Point out each malaria parasite.
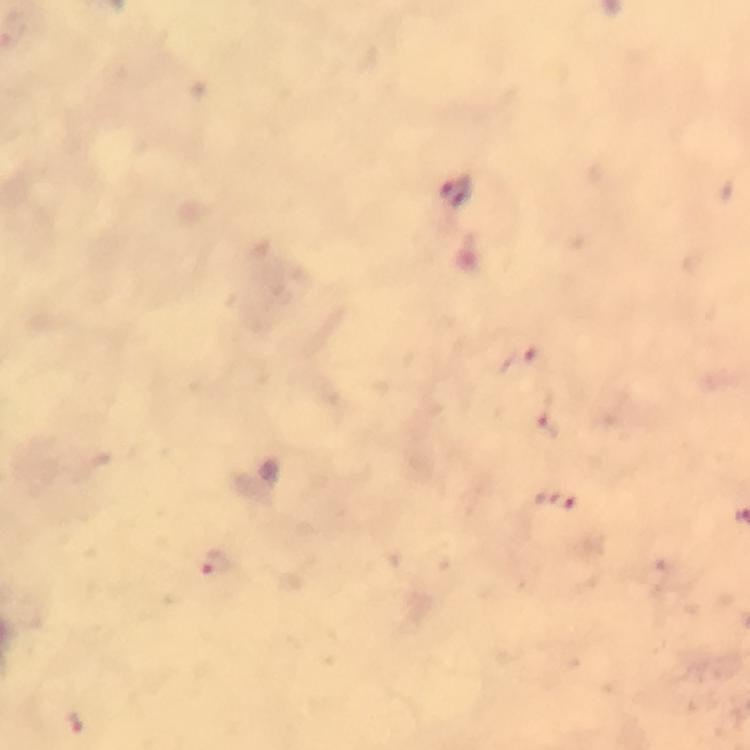
Approximate centers as (x, y) in pixels.
Malaria parasites: (457, 195), (521, 361), (546, 417), (557, 501), (215, 564), (73, 723).

Photographed with a smartphone mounted on the microscope. Giemsa stain. 100x magnification. Image is 750×750 pixels. A crop from one field of view. Immersion oil applied. Thick blood smear. From a diagnostic examination for malaria.